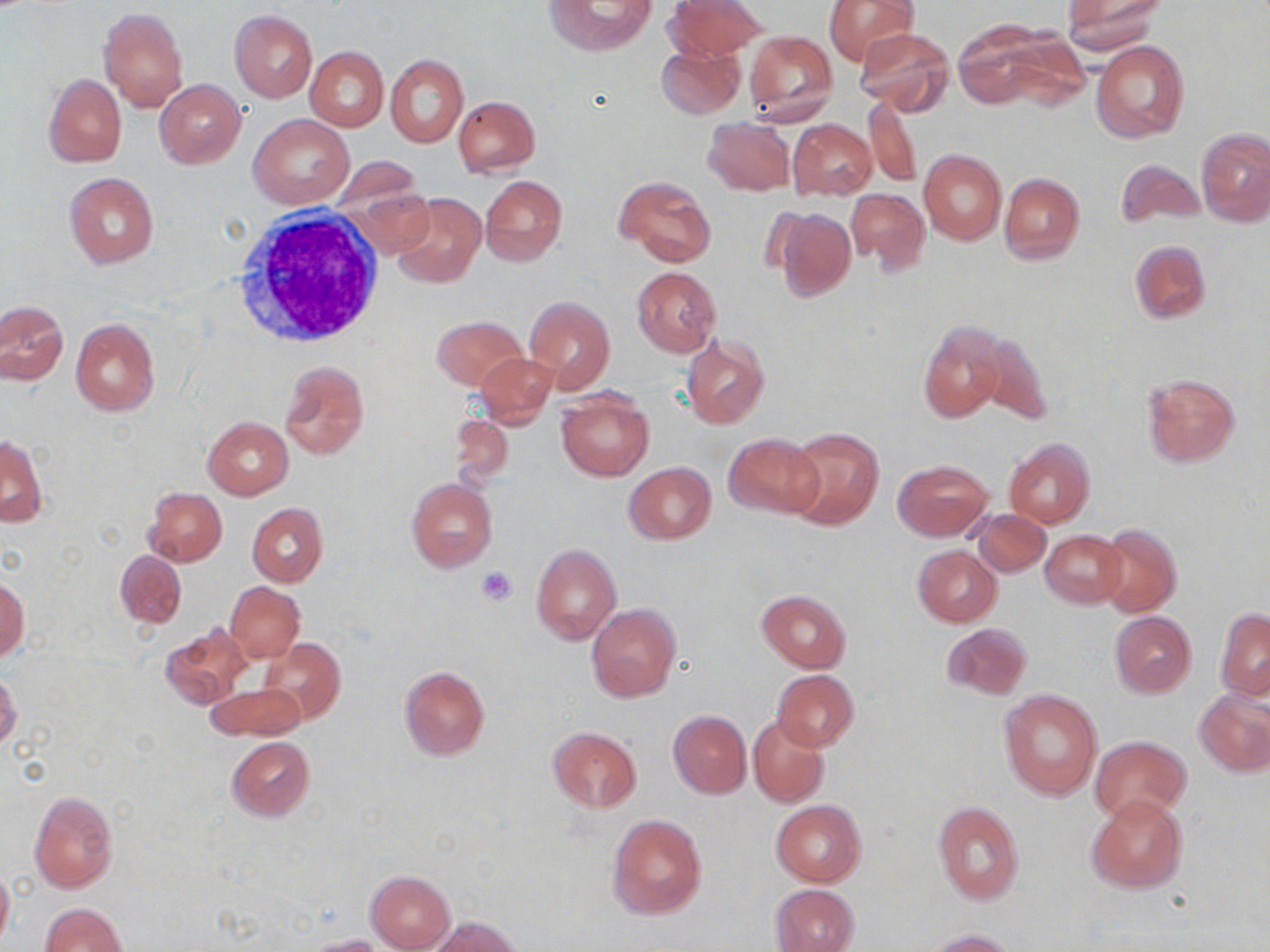

slide-level diagnosis = no evidence of blood parasites
white blood cell locations = approximate bounding boxes as (x1,y1)-(x2,y2) corner pairs in pixels: (226,210)-(385,348)
field of view = one of a larger specimen
preparation = thin blood film
uninfected red blood cell locations = approximate bounding boxes as (x1,y1)-(x2,y2) corner pairs in pixels: (547,0)-(654,54), (667,0)-(767,59), (823,0)-(917,66), (1061,1)-(1165,55), (99,7)-(189,112), (230,10)-(318,102), (952,20)-(1052,107), (853,26)-(954,116), (745,30)-(837,125), (999,32)-(1090,108), (1091,40)-(1189,144), (657,43)-(744,119), (305,46)-(388,130), (385,54)-(467,147), (44,73)-(127,168), (155,79)-(246,168), (862,93)-(922,188), (453,96)-(540,176), (251,114)-(355,208), (704,118)-(795,196), (787,119)-(877,200), (1197,127)-(1269,226), (918,148)-(1007,245), (1114,158)-(1204,229), (63,172)-(160,268), (342,172)-(433,254), (999,172)-(1086,264), (614,175)-(716,267), (479,176)-(568,265), (844,188)-(929,276), (391,193)-(486,288), (771,207)-(856,301), (1130,240)-(1211,324), (631,267)-(720,356), (525,295)-(617,393), (1,301)-(68,386), (432,315)-(526,390), (70,318)-(160,417), (917,321)-(1008,424), (964,324)-(1056,425), (681,335)-(771,431), (474,352)-(558,428), (278,359)-(370,461), (1141,372)-(1241,468), (556,390)-(653,481), (448,413)-(515,489), (203,417)-(294,500), (784,425)-(885,530), (723,432)-(826,519), (1,437)-(47,528), (1004,438)-(1094,529), (891,457)-(993,542), (623,462)-(716,544), (405,477)-(498,574), (143,487)-(227,566), (247,502)-(329,586), (973,508)-(1051,578), (1097,524)-(1182,618), (1040,530)-(1126,607), (531,543)-(622,645), (912,544)-(1002,627), (115,550)-(187,628), (0,577)-(29,663), (225,581)-(305,663), (755,589)-(851,672), (586,603)-(680,702), (1215,609)-(1270,700), (1109,611)-(1197,697), (940,622)-(1033,700), (160,625)-(253,709), (258,637)-(346,726), (398,666)-(490,759), (772,669)-(860,751), (0,672)-(22,750), (206,683)-(304,741), (1194,688)-(1270,777), (998,689)-(1103,800), (668,710)-(751,798), (748,714)-(831,808), (547,726)-(642,811), (1090,735)-(1190,822), (226,737)-(314,819), (28,790)-(118,894), (1086,793)-(1189,893), (770,800)-(867,887), (932,800)-(1025,907), (608,812)-(709,921), (0,864)-(13,949), (365,871)-(456,951), (769,883)-(859,952), (40,902)-(127,952), (429,916)-(524,952), (923,928)-(1022,952), (303,934)-(384,952)
stain = May-Grünwald-Giemsa
platelet locations = approximate bounding boxes as (x1,y1)-(x2,y2) corner pairs in pixels: (477,566)-(518,604)
magnification = 1000x
image size = 1270×952 pixels
modality = optical microscopy